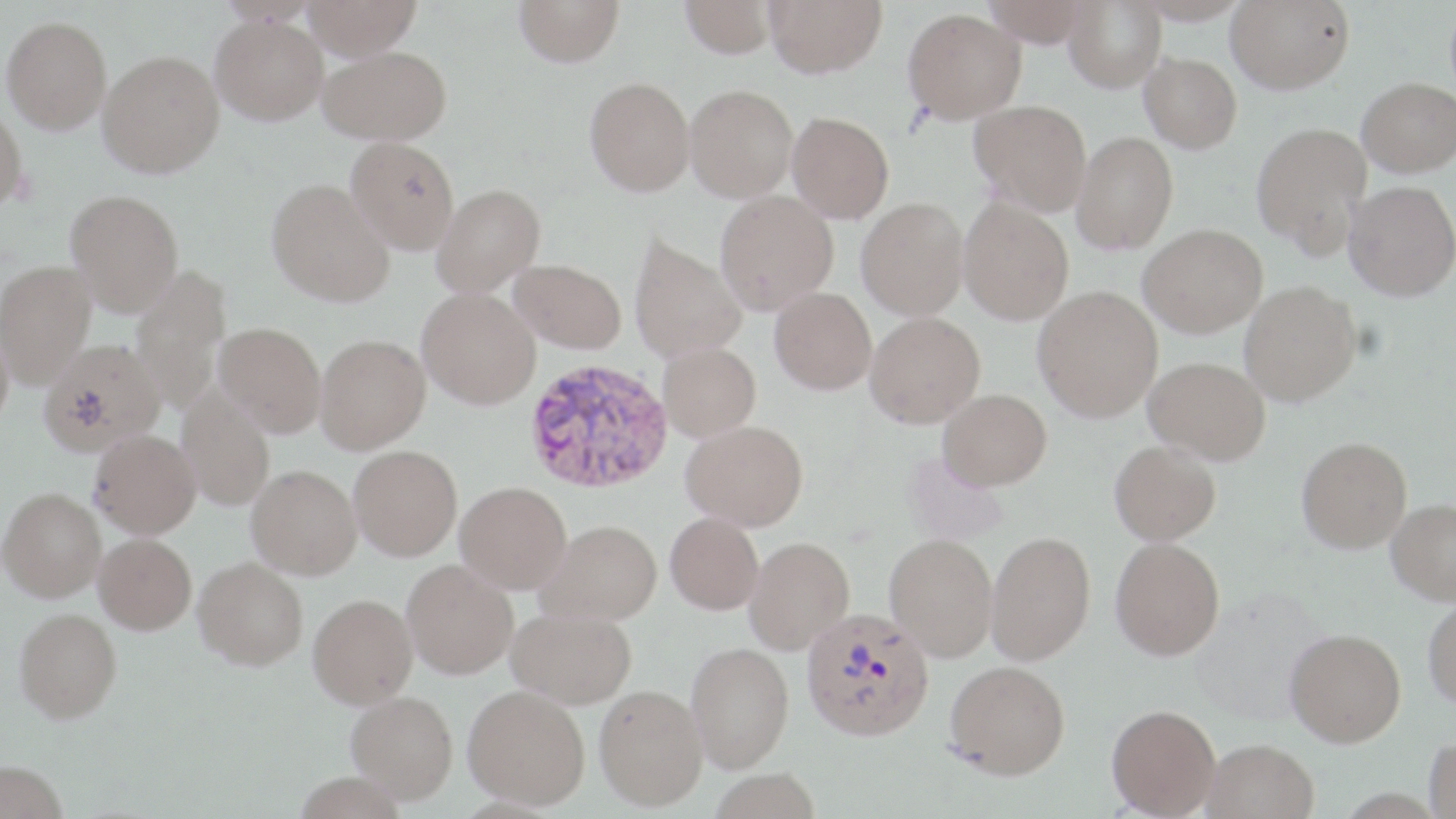 Approximate bounding boxes as (x1,y1)-(x2,y2) corner pairs in pixels. Uninfected red blood cell locations: (303,0)-(421,59), (514,0)-(624,67), (680,0)-(777,58), (764,0)-(887,77), (983,0)-(1094,48), (1064,0)-(1166,92), (1131,0)-(1253,24), (1226,0)-(1354,93), (903,8)-(1026,123), (211,14)-(328,125), (2,16)-(111,134), (318,46)-(451,144), (98,50)-(224,177), (1140,52)-(1242,153), (585,76)-(695,195), (1358,76)-(1456,177), (685,85)-(798,201), (970,99)-(1092,214), (0,105)-(28,211), (787,112)-(894,222), (1252,122)-(1372,257), (1072,132)-(1178,254), (346,137)-(459,254), (266,178)-(395,307), (1344,180)-(1456,300), (432,183)-(545,296), (65,189)-(184,315), (714,189)-(838,314), (856,197)-(969,320), (958,197)-(1074,325), (1139,223)-(1268,337), (629,233)-(746,363), (510,258)-(626,354), (1,259)-(96,388), (130,266)-(231,414), (1239,280)-(1362,406), (1033,285)-(1163,422), (416,287)-(541,409), (770,288)-(876,394), (865,312)-(985,428), (0,321)-(14,432), (215,322)-(326,437), (315,334)-(430,454), (39,338)-(165,455), (659,342)-(761,441), (1144,356)-(1270,464), (177,388)-(275,510), (938,389)-(1052,489), (682,420)-(808,531), (89,429)-(201,538), (1296,436)-(1412,553), (1109,440)-(1221,545), (348,445)-(462,560), (246,464)-(362,579), (455,481)-(572,594), (0,487)-(106,601), (1387,498)-(1456,605), (665,512)-(764,614), (538,520)-(662,625), (986,531)-(1095,664), (94,533)-(197,634), (885,534)-(998,660), (744,537)-(855,655), (1110,537)-(1225,660), (193,556)-(309,670), (402,559)-(518,679), (308,593)-(418,707), (1423,598)-(1456,708), (14,607)-(122,723), (507,607)-(637,708), (1285,628)-(1406,747), (686,642)-(794,772), (945,660)-(1070,779), (594,684)-(708,811), (463,685)-(590,808), (347,690)-(458,803), (1107,704)-(1221,817), (1425,735)-(1456,818), (1202,738)-(1319,819), (0,760)-(68,819). Plasmodium vivax-infected red blood cell locations: (523,358)-(674,495), (801,607)-(934,741). Slide-level diagnosis: Plasmodium vivax. Thin blood smear. Image is 1456×819 pixels. May-Grünwald-Giemsa stain. One field of a larger specimen. 1000x magnification. Optical microscopy.